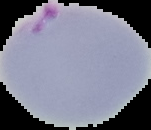 From a thin blood smear. Cell region segmented out of the field of view; the surrounding area is masked to black. Image is 151×130 pixels. Malaria status: parasitized.